Assess this cell for malaria.
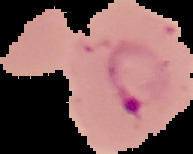

It is parasitized.

image_size: 193×154 pixels
preparation: thin blood film
image_type: cell region segmented out of the field of view; surrounding area masked to black